Give the extent of all Plasmodium malariae-infected red blood cells.
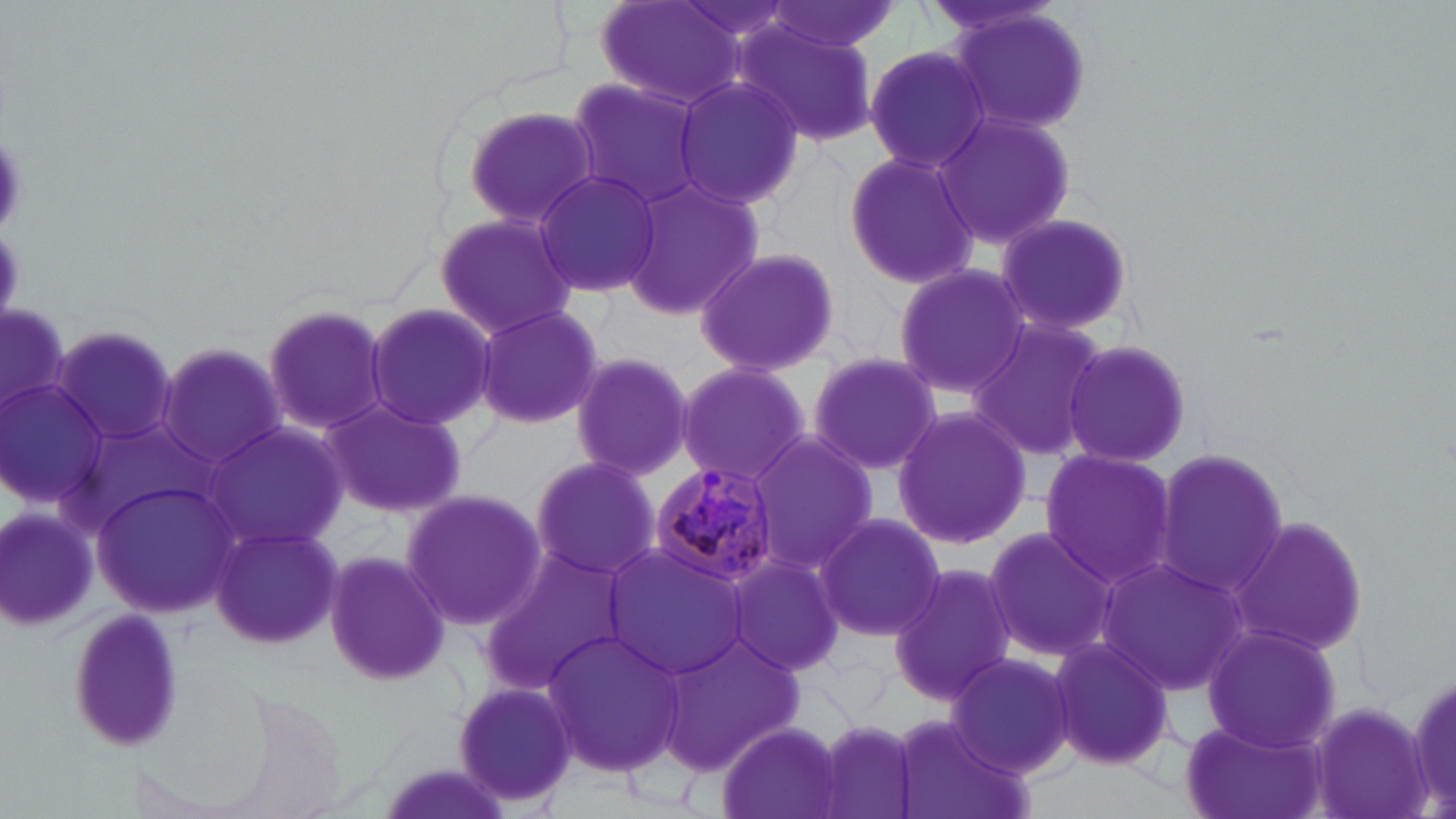
Approximate bounding boxes as named x1/y1/x2/y2 corners in pixels.
Plasmodium malariae-infected red blood cells: (x1=644, y1=462, x2=783, y2=586).

Summary:
  - Uninfected red blood cell locations: (x1=760, y1=1, x2=902, y2=59), (x1=593, y1=2, x2=746, y2=109), (x1=949, y1=8, x2=1095, y2=136), (x1=737, y1=23, x2=881, y2=148), (x1=864, y1=44, x2=993, y2=174), (x1=672, y1=75, x2=807, y2=210), (x1=565, y1=77, x2=709, y2=210), (x1=459, y1=104, x2=605, y2=231), (x1=935, y1=108, x2=1078, y2=250), (x1=841, y1=148, x2=982, y2=290), (x1=531, y1=167, x2=663, y2=299), (x1=619, y1=174, x2=766, y2=320), (x1=433, y1=210, x2=579, y2=341), (x1=992, y1=211, x2=1137, y2=338), (x1=693, y1=246, x2=841, y2=377), (x1=892, y1=264, x2=1031, y2=397), (x1=261, y1=301, x2=393, y2=440), (x1=363, y1=303, x2=497, y2=429), (x1=473, y1=304, x2=604, y2=428), (x1=966, y1=317, x2=1107, y2=463), (x1=53, y1=328, x2=180, y2=448), (x1=1059, y1=338, x2=1193, y2=468), (x1=158, y1=343, x2=290, y2=469), (x1=569, y1=349, x2=695, y2=482), (x1=807, y1=350, x2=945, y2=477), (x1=674, y1=362, x2=811, y2=488), (x1=0, y1=375, x2=114, y2=514), (x1=318, y1=397, x2=467, y2=518), (x1=895, y1=406, x2=1031, y2=549), (x1=202, y1=422, x2=348, y2=553), (x1=745, y1=432, x2=878, y2=572), (x1=1153, y1=447, x2=1288, y2=597), (x1=1038, y1=448, x2=1178, y2=589), (x1=527, y1=453, x2=661, y2=579), (x1=95, y1=478, x2=237, y2=613), (x1=402, y1=485, x2=549, y2=635), (x1=1, y1=506, x2=101, y2=631), (x1=814, y1=512, x2=947, y2=643), (x1=1231, y1=516, x2=1370, y2=657), (x1=209, y1=522, x2=342, y2=649), (x1=981, y1=526, x2=1114, y2=662), (x1=603, y1=542, x2=748, y2=680), (x1=478, y1=546, x2=638, y2=695), (x1=322, y1=549, x2=452, y2=688), (x1=725, y1=553, x2=847, y2=676), (x1=1098, y1=556, x2=1249, y2=693), (x1=888, y1=562, x2=1018, y2=705), (x1=1203, y1=624, x2=1343, y2=753), (x1=543, y1=628, x2=685, y2=778), (x1=661, y1=629, x2=807, y2=770), (x1=1049, y1=636, x2=1175, y2=769), (x1=944, y1=651, x2=1076, y2=779), (x1=451, y1=681, x2=578, y2=808), (x1=1309, y1=700, x2=1432, y2=817), (x1=813, y1=717, x2=920, y2=819), (x1=888, y1=717, x2=1031, y2=819), (x1=1177, y1=719, x2=1327, y2=819), (x1=715, y1=721, x2=842, y2=819), (x1=372, y1=759, x2=516, y2=819)
  - Slide-level diagnosis: Plasmodium malariae
  - Modality: optical microscopy
  - Preparation: thin blood film
  - Field of view: one of a larger specimen
  - Magnification: 1000x
  - Stain: May-Grünwald-Giemsa
  - Image size: 1456×819 pixels